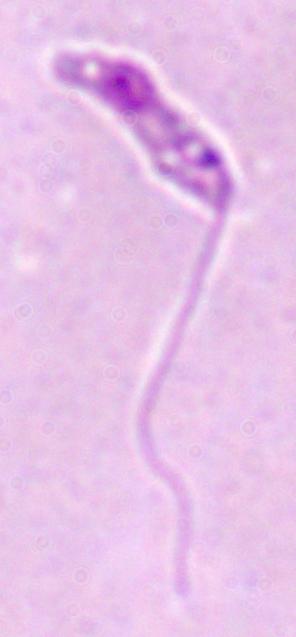
Summary:
  - Identification: Leishmania
  - Magnification: 1000x
  - Modality: photomicrograph